Classify this cell by malaria status.
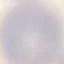

It is uninfected.

image type = cell patch, automatically extracted from a larger field of view and resized to 64 × 64 pixels
stain = Giemsa
capture = smartphone through the microscope eyepiece
preparation = thin blood smear